Classify this cell by malaria status.
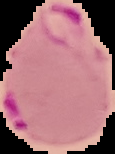

Parasitized.

Summary:
  - Image size: 115×154 pixels
  - Image type: segmented cell region on a black background
  - Preparation: thin blood film